Locate every Plasmodium parasite.
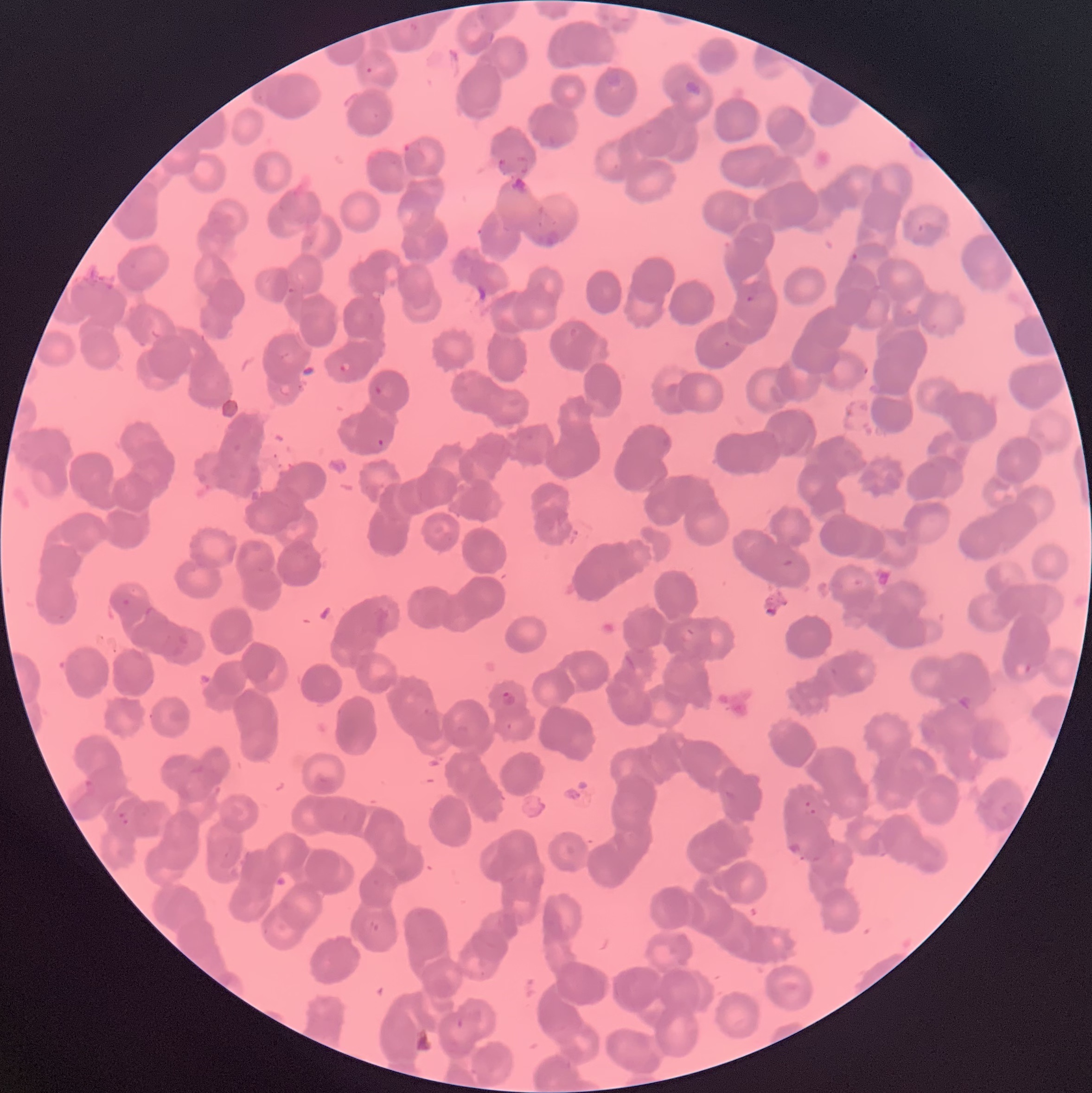
Approximate bounding boxes as (x1,y1)-(x2,y2) corner pairs in pixels.
Plasmodium parasites: (365,67)-(373,74), (682,80)-(704,97), (403,142)-(413,155), (917,224)-(924,233), (849,252)-(861,262), (745,296)-(755,303), (337,361)-(353,373), (862,363)-(870,377), (373,383)-(385,395), (377,438)-(385,447), (121,597)-(131,608), (1013,661)-(1032,678), (500,690)-(517,708), (83,774)-(98,794), (800,799)-(818,816), (117,811)-(130,825).
Plasmodium parasites too small for a box (approximate centers as (x,y) in pixels): (726,343).

red blood cell morphology = rouleaux formation
preparation = thin blood smear
modality = light microscopy
image size = 1092×1093 pixels